Evaluate for malaria.
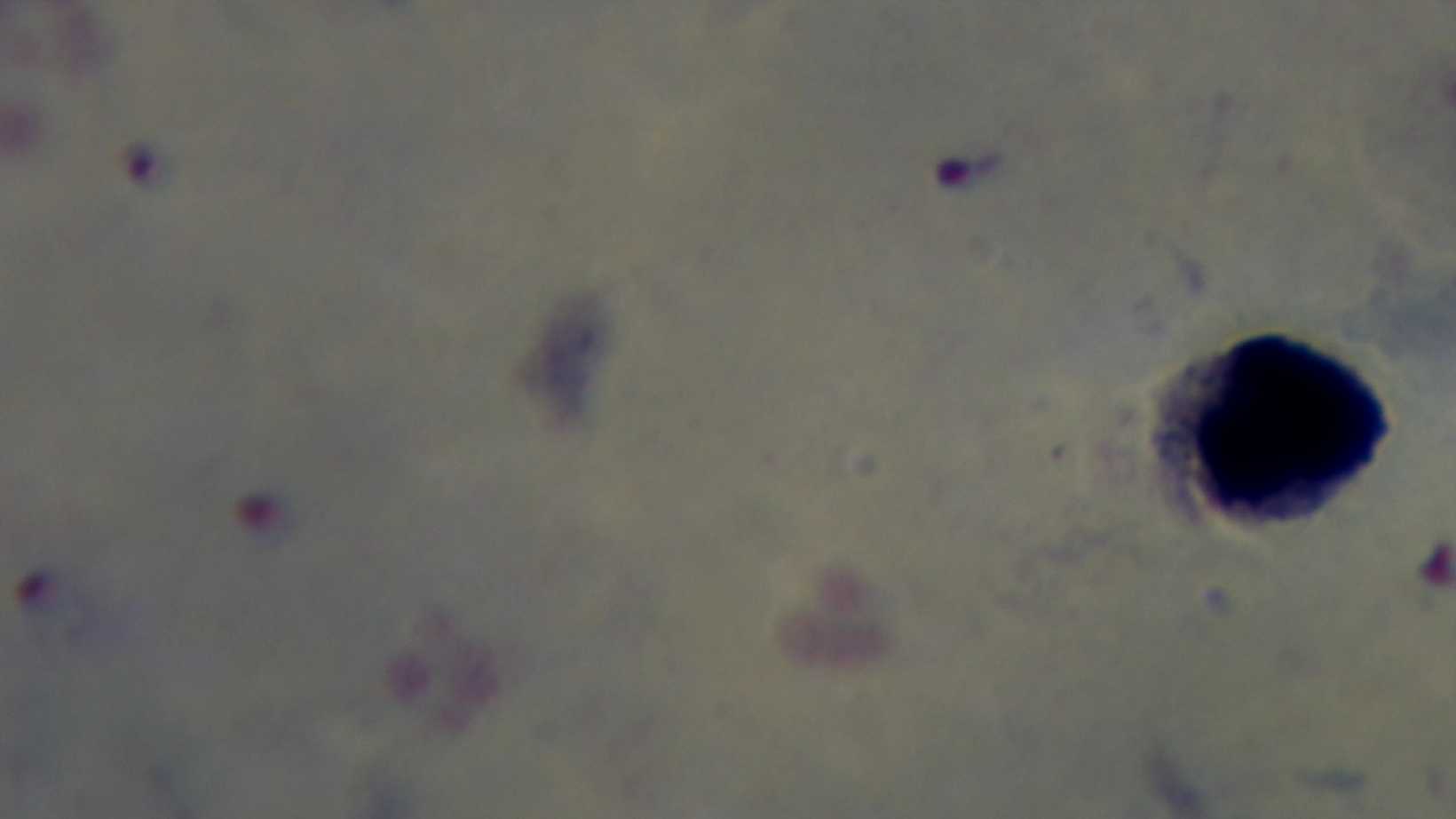

Infected.

field_of_view: single
objective: 100x oil immersion
capture: mounted 4K digital camera
stain: Giemsa
preparation: thick smear
modality: light microscopy